Locate every blood parasite and identify its species.
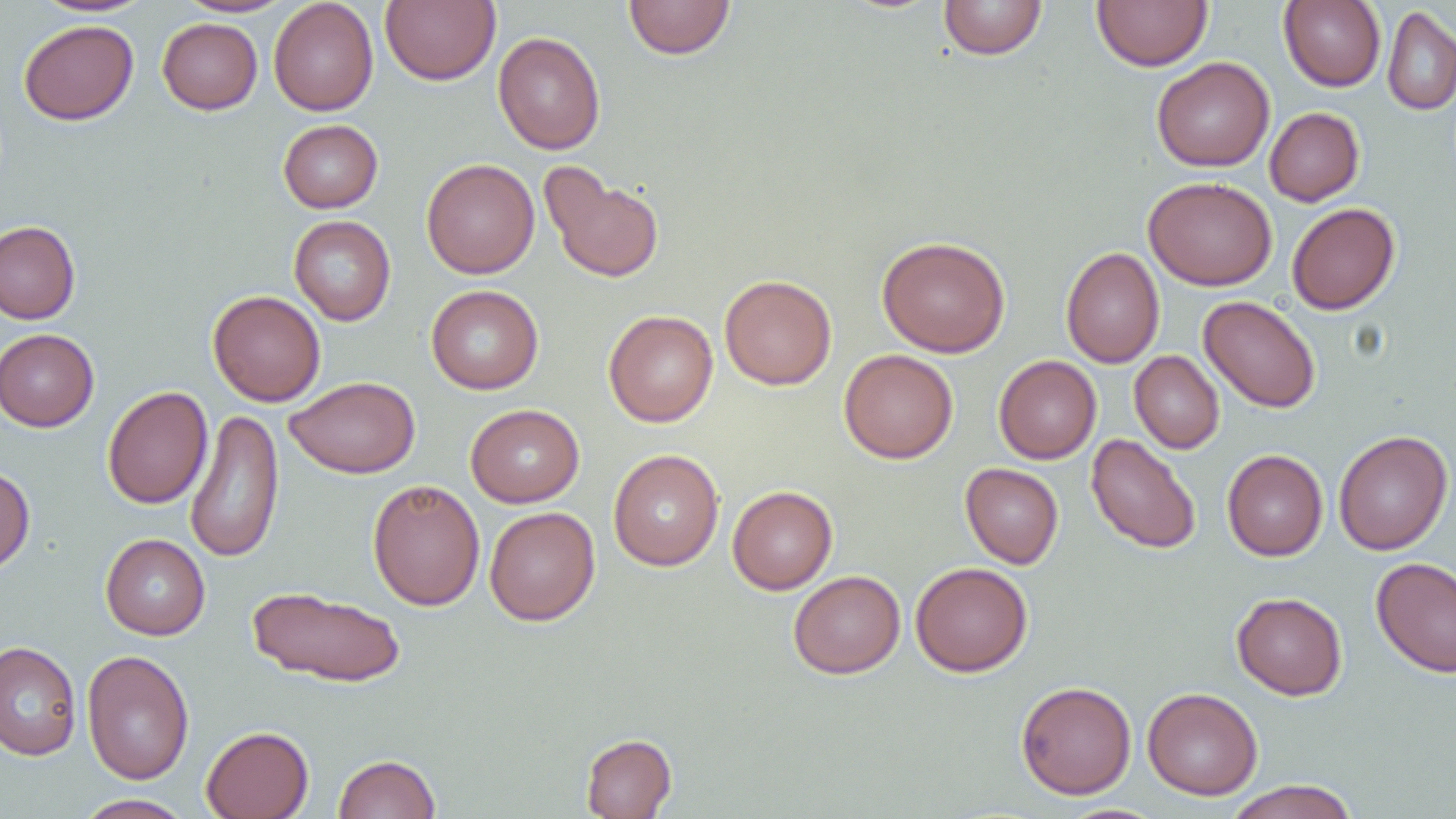
No blood parasites seen.

slide-level diagnosis = negative for blood parasites
preparation = thin blood film
modality = optical microscopy
magnification = 1000x
uninfected red blood cell locations = approximate bounding boxes as [x1, y1, x2, y2] in pixels: [32, 0, 155, 17], [177, 0, 294, 17], [268, 0, 379, 116], [380, 0, 500, 86], [623, 0, 735, 59], [938, 0, 1048, 60], [1091, 0, 1213, 71], [1279, 0, 1386, 91], [1382, 5, 1456, 115], [157, 18, 262, 114], [18, 19, 139, 125], [493, 31, 606, 154], [1151, 56, 1275, 172], [1265, 107, 1364, 206], [278, 119, 383, 213], [421, 158, 539, 279], [540, 163, 665, 284], [1143, 176, 1277, 290], [1286, 202, 1400, 315], [289, 215, 396, 325], [0, 220, 81, 325], [877, 235, 1010, 357], [1061, 246, 1164, 368], [720, 274, 837, 390], [426, 284, 544, 394], [207, 290, 326, 406], [1198, 296, 1321, 413], [603, 310, 718, 427], [0, 328, 99, 431], [839, 349, 959, 464], [1129, 351, 1225, 454], [994, 355, 1101, 464], [284, 375, 420, 478], [102, 386, 213, 509], [465, 404, 584, 507], [185, 409, 285, 563], [1333, 430, 1453, 555], [1086, 433, 1202, 554], [608, 449, 724, 571], [1222, 449, 1328, 560], [960, 463, 1064, 569], [0, 464, 35, 575], [367, 479, 485, 611], [727, 485, 837, 594], [484, 506, 600, 625], [100, 533, 210, 640], [1371, 556, 1456, 678], [910, 561, 1033, 677], [788, 570, 905, 679], [246, 585, 407, 687], [1231, 592, 1348, 700], [0, 641, 81, 761], [82, 649, 194, 785], [1015, 680, 1137, 799], [1142, 687, 1263, 800], [201, 725, 314, 819], [581, 733, 677, 818], [333, 753, 440, 818], [1223, 780, 1360, 819], [74, 794, 193, 818], [1055, 804, 1169, 819]
image size = 1456×819 pixels
field of view = one of a larger specimen